Assess the morphology of the erythrocytes.
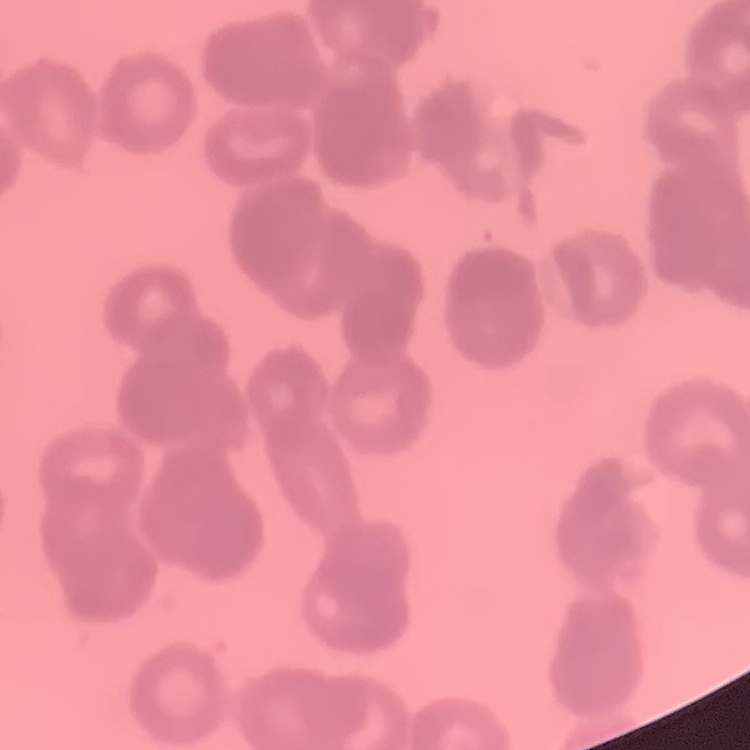
They show rouleaux formation.

Summary:
  - Preparation: thin blood film
  - Image type: square crop of a larger photomicrograph
  - Stain: Field's or Giemsa